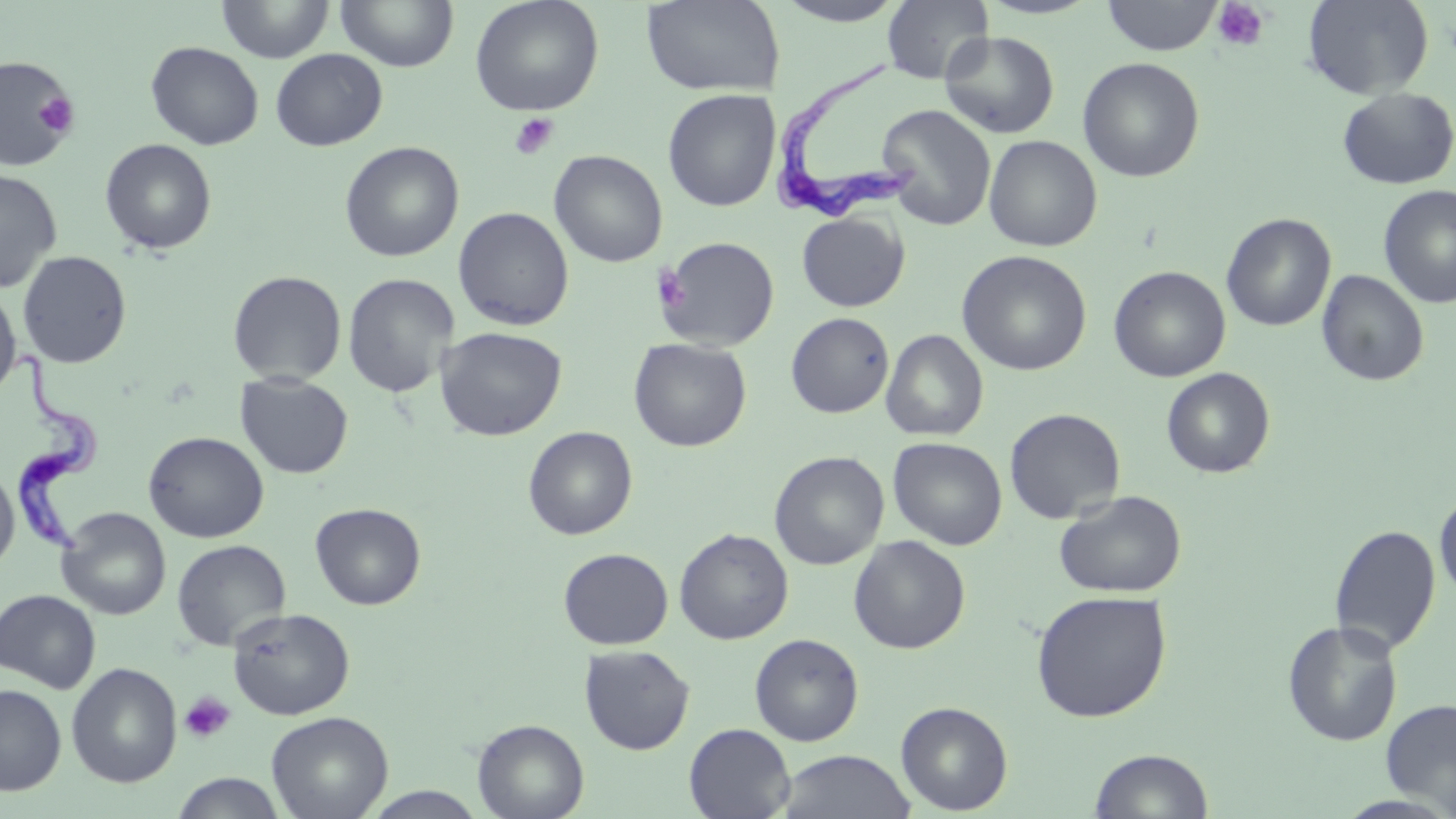
Approximate bounding boxes as [x1, y1, x2, y2] in pixels. Trypanosoma brucei locations: [772, 48, 923, 224], [11, 349, 102, 567]. Uninfected red blood cell locations: [216, 0, 335, 63], [336, 0, 459, 72], [470, 0, 604, 116], [641, 0, 784, 97], [770, 0, 911, 27], [881, 0, 992, 83], [1101, 0, 1223, 56], [1303, 0, 1434, 99], [939, 31, 1059, 139], [146, 42, 264, 149], [270, 48, 387, 151], [0, 55, 79, 170], [1077, 57, 1205, 182], [1337, 87, 1455, 189], [662, 88, 781, 212], [876, 105, 996, 231], [983, 135, 1102, 252], [100, 138, 217, 255], [339, 141, 464, 262], [549, 150, 667, 268], [0, 169, 62, 293], [1378, 185, 1456, 308], [453, 206, 574, 331], [796, 212, 909, 312], [1221, 213, 1336, 331], [656, 236, 780, 351], [17, 250, 133, 368], [957, 250, 1092, 376], [1108, 265, 1231, 382], [227, 270, 347, 385], [1316, 270, 1429, 387], [343, 273, 459, 397], [0, 286, 21, 401], [786, 312, 894, 418], [434, 326, 567, 441], [881, 329, 988, 441], [628, 338, 752, 452], [1160, 367, 1275, 478], [235, 373, 353, 479], [1004, 407, 1125, 524], [523, 426, 638, 540], [143, 431, 269, 542], [888, 436, 1007, 550], [769, 450, 889, 570], [0, 463, 19, 575], [1054, 489, 1187, 598], [1434, 490, 1456, 601], [310, 503, 426, 610], [57, 507, 171, 620], [1330, 524, 1441, 656], [674, 528, 794, 644], [848, 535, 971, 654], [171, 539, 291, 651], [558, 547, 673, 650], [0, 589, 102, 693], [1031, 590, 1172, 722], [227, 607, 354, 720], [1281, 619, 1403, 747], [749, 633, 864, 746], [579, 644, 695, 755], [66, 662, 182, 788], [0, 684, 66, 795], [1380, 698, 1456, 815], [895, 701, 1013, 814], [266, 710, 393, 819], [473, 718, 589, 819], [683, 723, 795, 819], [1089, 748, 1214, 818], [775, 749, 917, 818], [170, 772, 287, 818], [361, 787, 489, 818]. Platelet locations: [1212, 1, 1270, 52], [0, 62, 82, 161], [37, 92, 79, 138], [508, 113, 559, 160], [653, 266, 690, 313], [180, 691, 235, 744]. Slide-level diagnosis: Trypanosoma brucei. May-Grünwald-Giemsa stain. Image is 1456×819 pixels. Thin blood film. Captured at 1000x magnification. Optical microscopy. Single field of view.